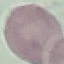
{
  "result": "no malaria parasites seen",
  "stain": "Giemsa",
  "preparation": "thin blood smear",
  "capture": "smartphone through the microscope eyepiece",
  "image_type": "cell patch, automatically extracted from a larger field of view and resized to 64 × 64 pixels"
}